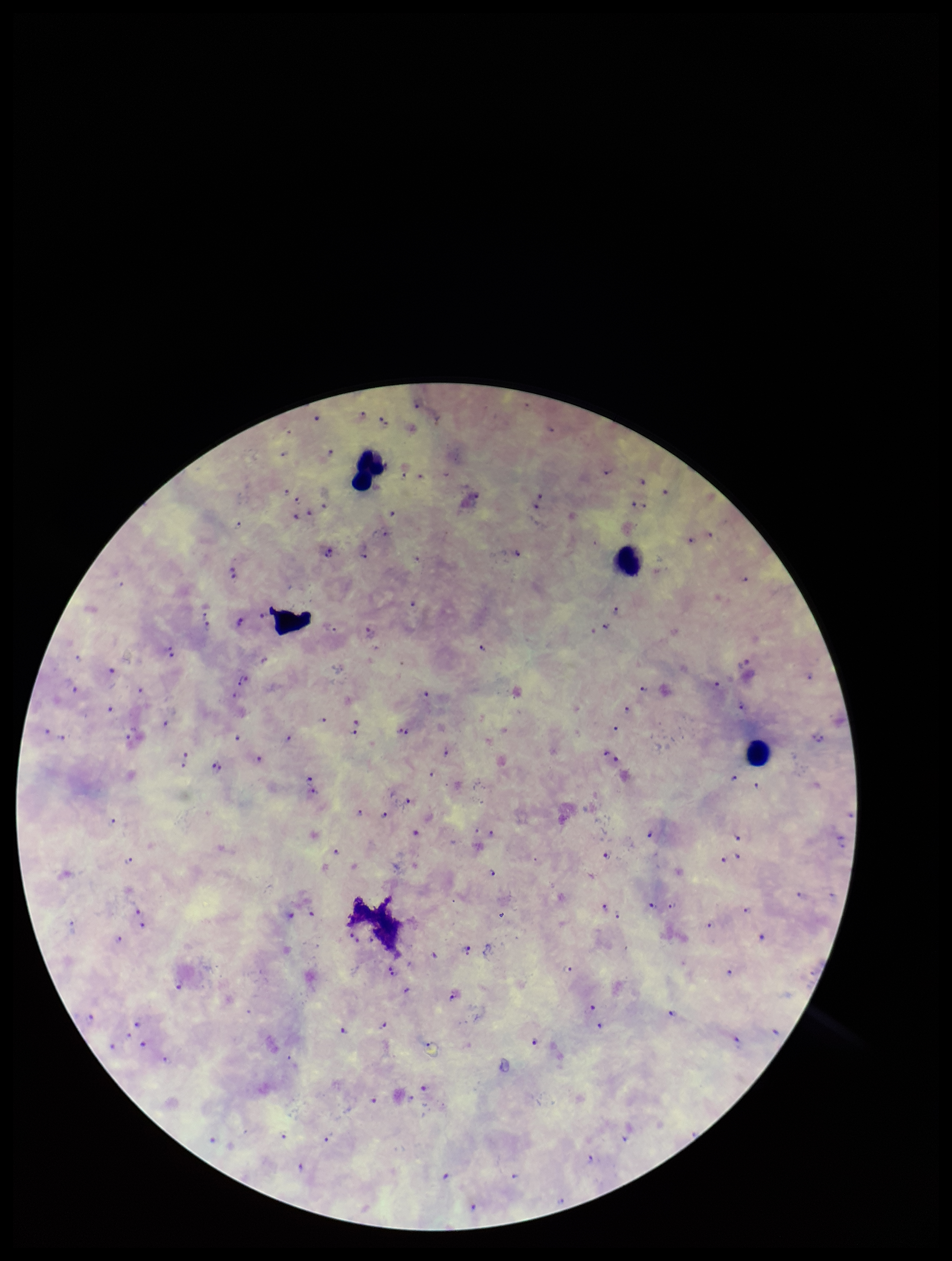

capture = smartphone photograph through the microscope eyepiece
leukocyte count = 4
Plasmodium parasites = detected
patient malaria status = positive
image size = 952×1261 pixels
species reported for this patient = Plasmodium falciparum
parasite count = 121
stain = Giemsa
preparation = thick blood smear
field of view = one from this slide